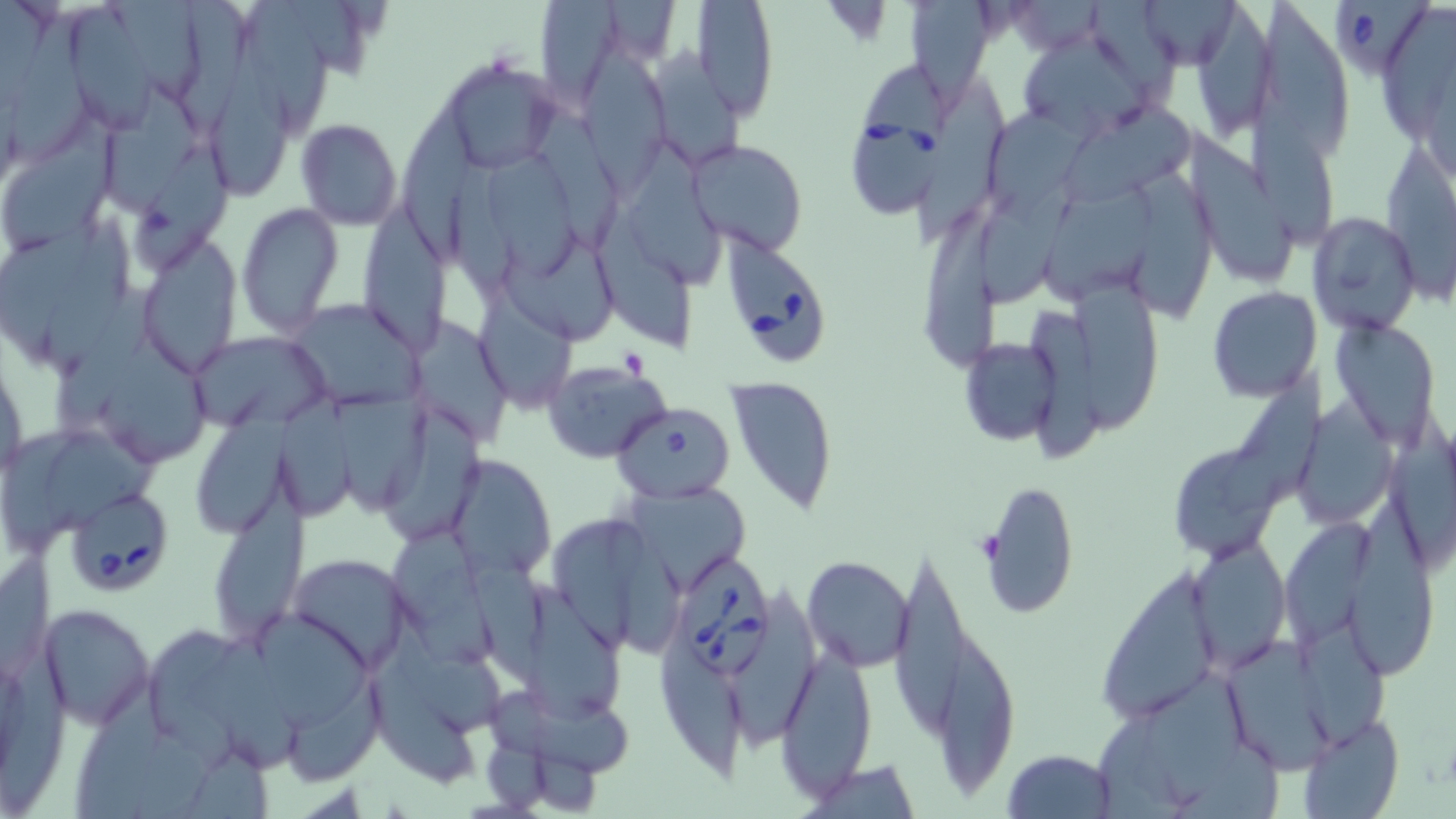 Approximate bounding boxes as (x1,y1)-(x2,y2) corner pairs in pixels. Uninfected red blood cell locations: (112,0)-(202,101), (180,0)-(250,137), (245,0)-(329,139), (291,0)-(374,81), (535,0)-(629,105), (691,0)-(779,121), (1137,0)-(1240,69), (1264,0)-(1351,161), (906,1)-(1000,98), (1191,1)-(1281,140), (72,5)-(157,135), (1380,6)-(1456,152), (8,8)-(91,171), (1016,26)-(1163,141), (211,27)-(292,198), (652,46)-(750,166), (578,49)-(670,196), (436,56)-(563,175), (914,75)-(1007,248), (107,81)-(203,214), (991,102)-(1092,219), (1247,104)-(1335,249), (1063,105)-(1201,207), (536,112)-(625,250), (400,113)-(481,259), (5,117)-(120,254), (294,118)-(403,231), (1188,127)-(1296,285), (687,138)-(807,257), (1384,139)-(1456,309), (129,143)-(232,273), (621,148)-(722,290), (491,156)-(585,275), (449,162)-(519,309), (1136,166)-(1212,319), (980,173)-(1084,306), (1039,181)-(1156,304), (360,200)-(447,357), (237,202)-(342,338), (928,204)-(999,371), (0,212)-(108,373), (1308,212)-(1421,337), (599,215)-(690,358), (42,216)-(137,379), (138,238)-(243,373), (501,248)-(614,346), (64,283)-(155,430), (1075,284)-(1155,434), (1207,286)-(1322,402), (477,290)-(575,414), (285,298)-(426,410), (1024,300)-(1098,467), (1331,319)-(1441,445), (414,320)-(515,447), (191,331)-(332,433), (959,337)-(1061,446), (105,342)-(208,460), (543,360)-(669,462), (1220,364)-(1327,521), (725,374)-(839,516), (194,386)-(299,538), (276,392)-(357,521), (334,395)-(435,522), (1296,396)-(1402,530), (380,405)-(494,543), (1388,410)-(1456,578), (3,427)-(86,555), (53,438)-(155,525), (1167,442)-(1284,562), (448,455)-(556,581), (980,479)-(1080,619), (622,482)-(752,595), (1356,503)-(1435,679), (209,510)-(307,647), (546,510)-(680,653), (1280,517)-(1376,642), (459,530)-(550,688), (392,532)-(495,663), (1189,534)-(1289,672), (0,551)-(61,679), (288,554)-(415,671), (892,555)-(966,728), (802,556)-(914,671), (1091,565)-(1222,727), (735,587)-(825,754), (525,588)-(623,719), (40,604)-(153,728), (262,615)-(372,730), (1291,620)-(1386,758), (936,624)-(1014,795), (660,630)-(744,778), (0,637)-(68,814), (192,638)-(305,774), (1223,639)-(1341,773), (776,647)-(877,797), (372,662)-(470,795), (1134,667)-(1251,807), (291,676)-(384,783), (76,685)-(168,819), (489,688)-(638,780), (1297,716)-(1405,819), (482,736)-(550,813), (528,747)-(602,813), (1001,748)-(1118,819), (806,758)-(919,819). Babesia divergens-infected red blood cell locations: (1337,2)-(1430,78), (851,69)-(948,218), (724,239)-(826,368), (611,403)-(736,501), (72,498)-(168,589), (669,550)-(778,677). Slide-level diagnosis: Babesia divergens. May-Grünwald-Giemsa-stained preparation. Light microscopy. Image is 1456×819 pixels. 1000x magnification. Thin blood smear. Single field of view.